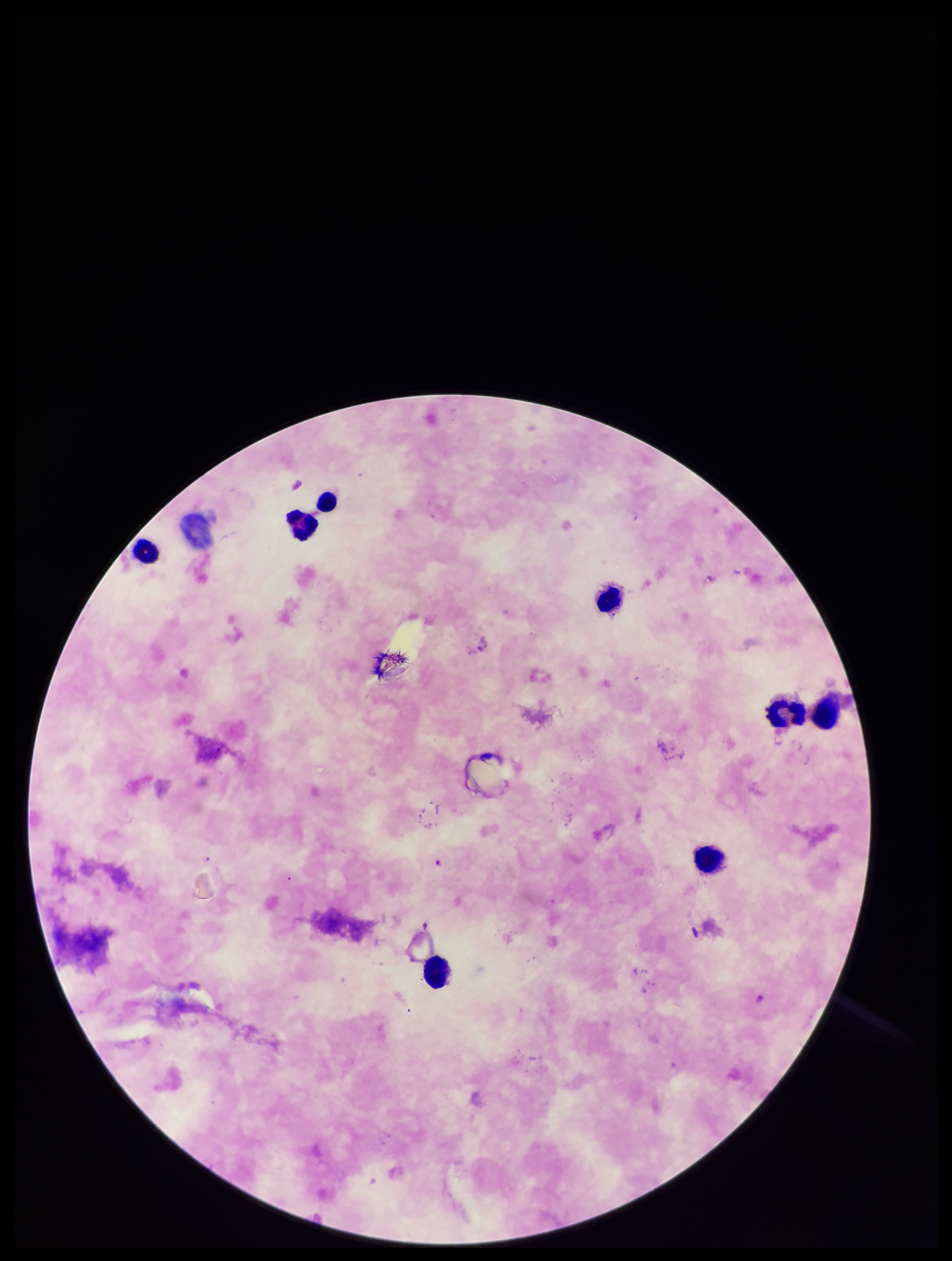

Summary:
  - Patient malaria status: infected
  - Plasmodium parasites: none seen
  - Leukocyte count: 8
  - Capture: smartphone photograph through the microscope eyepiece
  - Stain: Giemsa
  - Preparation: thick blood smear
  - Species reported for this patient: Plasmodium falciparum
  - Image size: 952×1261 pixels
  - Parasite count: 0
  - Field of view: one from this slide